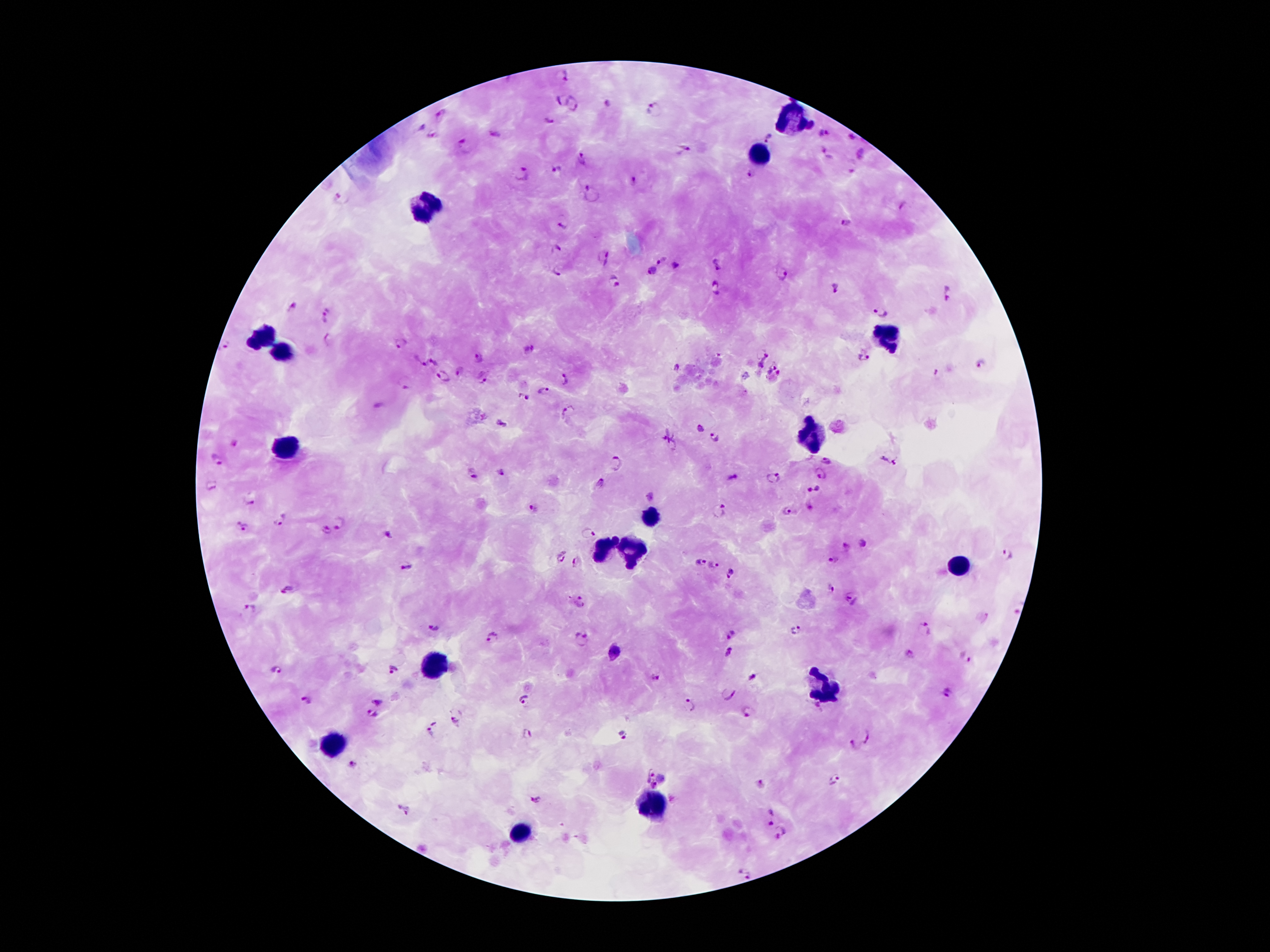

coordinate format = approximate centers as [x, y] in pixels
leukocyte locations = [793, 118], [759, 156], [422, 206], [263, 336], [885, 338], [282, 351], [815, 431], [290, 448], [648, 518], [601, 549], [634, 551], [961, 568], [433, 665], [826, 691], [331, 743], [655, 803], [522, 833]
malaria parasite locations = [562, 76], [560, 99], [573, 104], [608, 105], [652, 110], [440, 115], [548, 121], [420, 127], [823, 134], [495, 135], [430, 137], [768, 138], [850, 138], [466, 146], [684, 148], [823, 150], [863, 156], [582, 159], [556, 169], [521, 174], [750, 176], [634, 183], [592, 194], [340, 198], [903, 206], [845, 223], [563, 224], [557, 248], [604, 256], [660, 260], [675, 264], [716, 266], [652, 271], [782, 272], [556, 273], [614, 282], [716, 288], [835, 289], [948, 293], [292, 306], [881, 313], [328, 314], [328, 340], [401, 342], [226, 345], [531, 349], [759, 352], [479, 357], [864, 357], [435, 362], [422, 363], [981, 364], [771, 365], [676, 368], [462, 370], [443, 374], [938, 374], [484, 378], [565, 380], [405, 381], [544, 391], [524, 396], [568, 412], [502, 422], [699, 430], [716, 438], [669, 440], [825, 460], [889, 460], [217, 461], [616, 462], [821, 473], [501, 475], [773, 476], [472, 478], [732, 478], [600, 482], [210, 485], [813, 488], [249, 500], [532, 508], [718, 512], [788, 512], [282, 520], [340, 523], [236, 524], [245, 528], [326, 531], [588, 533], [388, 535], [1006, 553], [560, 555], [835, 559], [576, 562], [699, 562], [407, 565], [713, 566], [730, 574], [832, 588], [287, 589], [851, 598], [579, 601], [249, 608], [432, 626], [923, 628], [795, 630], [731, 634], [492, 637], [581, 640], [613, 652], [729, 652], [910, 654], [965, 658], [277, 668], [393, 669], [753, 676], [656, 678], [948, 692], [729, 694], [524, 699], [306, 701], [379, 701], [690, 704], [749, 712], [373, 715], [456, 722], [432, 727], [527, 735], [622, 736], [867, 737], [850, 746], [354, 766], [647, 774], [835, 780], [656, 785], [761, 785], [537, 799], [404, 811], [769, 818], [784, 835], [743, 873]
preparation = thick blood smear
magnification = 100x
stain = Giemsa
capture = smartphone camera through the microscope eyepiece
field of view = single
image size = 1270×952 pixels
patient malaria status = positive for Plasmodium falciparum